Assess this cell for malaria.
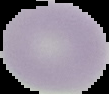
It is uninfected.

Cell region segmented out of the field of view; the surrounding area is masked to black. From a thin blood film. Image is 109×94 pixels.